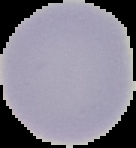

Summary:
  - Image size: 136×148 pixels
  - Image type: segmented cell region on a black background
  - Preparation: thin blood film
  - Malaria status: uninfected